Give the position of every Plasmodium parasite.
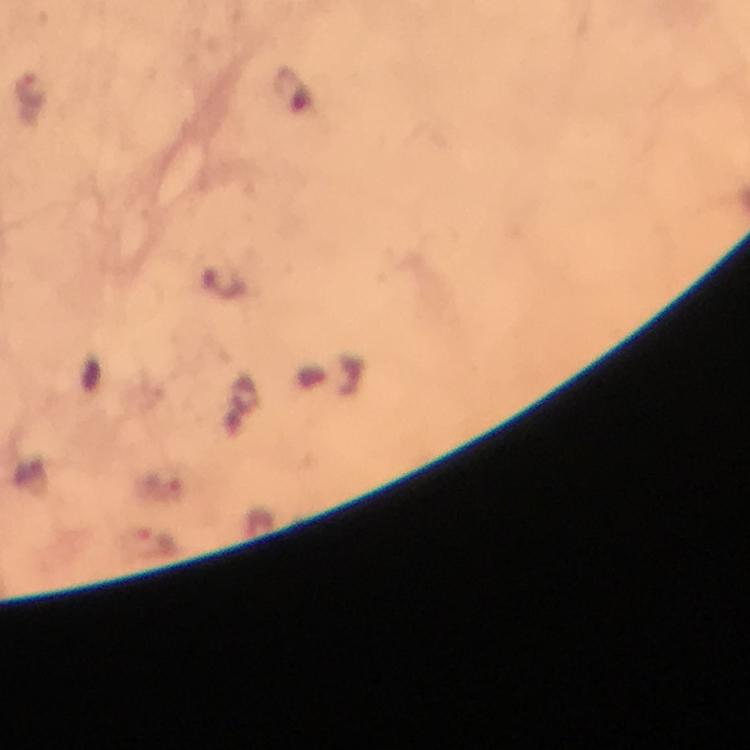

Approximate object centers, in pixels from the top-left corner.
Plasmodium parasites: (x=156, y=541).

Giemsa-stained preparation. 100x magnification. Smartphone photograph taken through a microscope. Thick blood smear. From a diagnostic examination for malaria. Cropped region of a single field of view. Immersion oil was used. Image is 750×750 pixels.